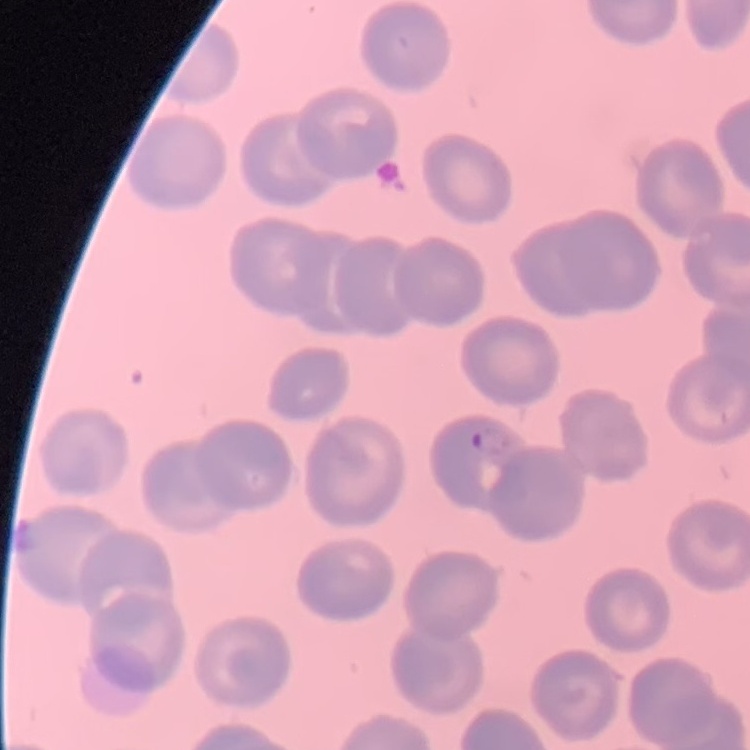
The erythrocytes exhibit no rouleaux formation. Stained with either Field's or Giemsa. One tile cut from a larger photomicrograph. Thin blood smear.